Name the parasite shown.
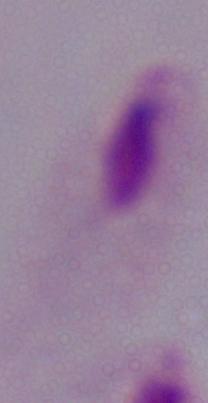

This is a trichomonad.

Micrograph. 1000x magnification.